Classify this cell by malaria status.
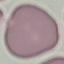

It is uninfected.

Automatically extracted cell patch, resized to 64 × 64 pixels. Acquired by smartphone through the microscope eyepiece. Thin smear of blood. Giemsa stain.